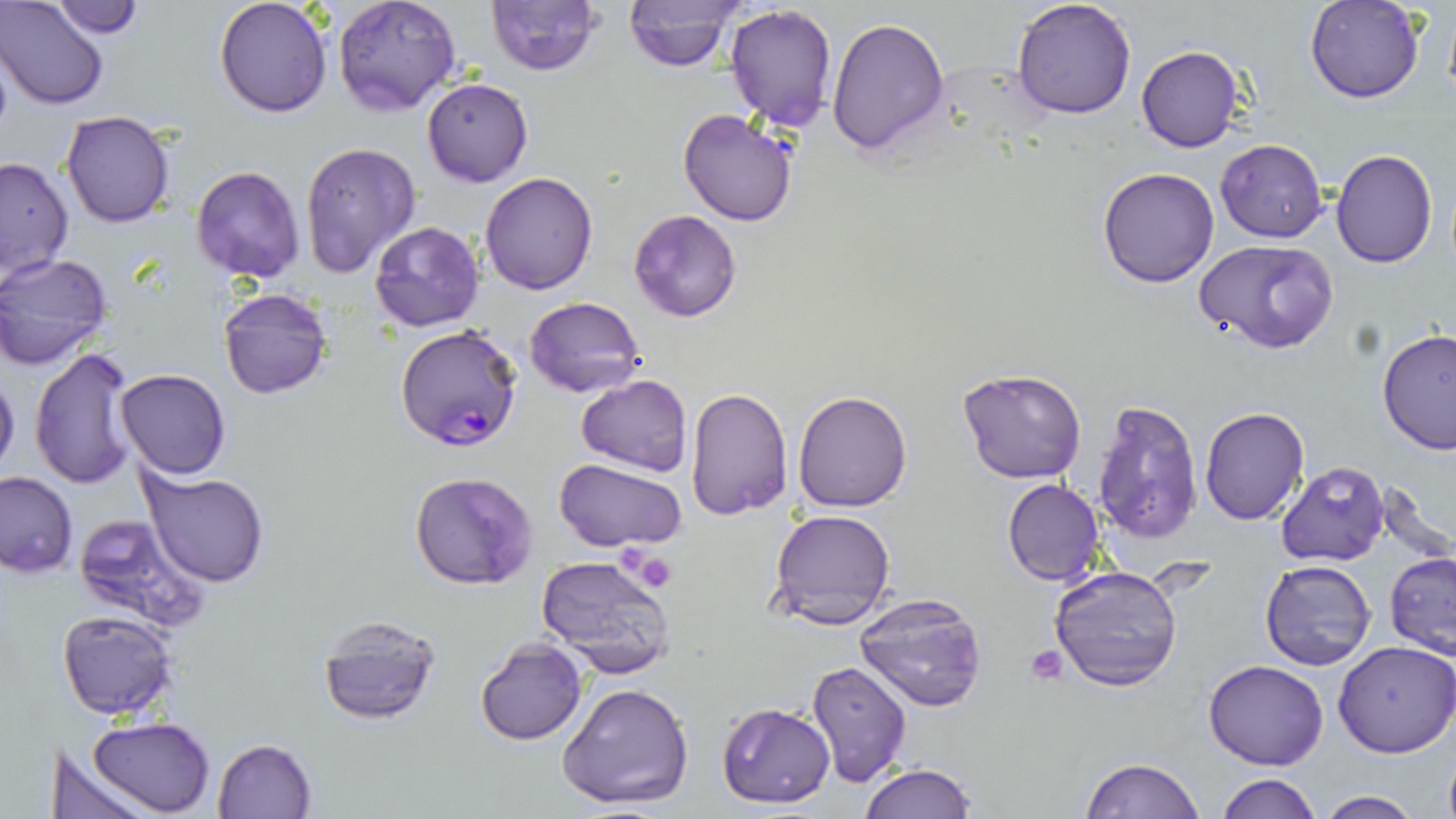

Approximate bounding boxes as (x1,y1)-(x2,y2) corner pairs in pixels. Plasmodium falciparum-infected red blood cell locations: (396,324)-(522,452). Uninfected red blood cell locations: (1,0)-(109,108), (214,0)-(335,117), (332,0)-(461,117), (486,0)-(599,75), (1011,0)-(1138,120), (1304,0)-(1425,103), (51,2)-(145,39), (621,2)-(745,73), (723,4)-(837,133), (826,17)-(950,156), (1135,44)-(1244,154), (421,78)-(533,187), (677,109)-(798,227), (60,110)-(174,228), (1214,138)-(1326,241), (298,142)-(421,280), (1330,147)-(1439,268), (0,156)-(74,283), (191,164)-(305,283), (1097,167)-(1219,288), (481,173)-(598,294), (629,210)-(742,322), (369,221)-(485,331), (1194,239)-(1338,354), (0,253)-(114,370), (217,286)-(334,399), (525,295)-(646,400), (1377,329)-(1456,455), (28,346)-(141,489), (116,367)-(231,479), (956,367)-(1087,484), (0,368)-(20,483), (575,374)-(692,474), (685,386)-(793,520), (792,389)-(915,513), (1091,398)-(1203,547), (1199,406)-(1310,526), (555,459)-(688,552), (1275,463)-(1390,567), (140,469)-(271,588), (0,470)-(78,576), (409,470)-(539,592), (1002,479)-(1106,586), (767,508)-(897,632), (73,512)-(211,633), (1384,551)-(1456,656), (536,555)-(675,675), (1261,561)-(1376,670), (1049,564)-(1183,690), (855,591)-(988,712), (57,610)-(178,720), (316,613)-(441,724), (475,638)-(587,746), (1332,639)-(1456,757), (1204,658)-(1329,770), (806,660)-(911,786), (557,680)-(696,811), (717,701)-(835,808), (87,716)-(216,817), (211,738)-(318,819), (52,742)-(150,819), (1441,745)-(1456,819), (1080,757)-(1203,819), (860,762)-(976,819), (1214,775)-(1323,818), (1315,791)-(1427,818). Platelet locations: (623,548)-(679,591), (1026,643)-(1070,685). Slide-level diagnosis: Plasmodium falciparum. May-Grünwald-Giemsa stain. Image is 1456×819 pixels. 1000x magnification. Single field of view. Light microscopy. Thin blood smear.